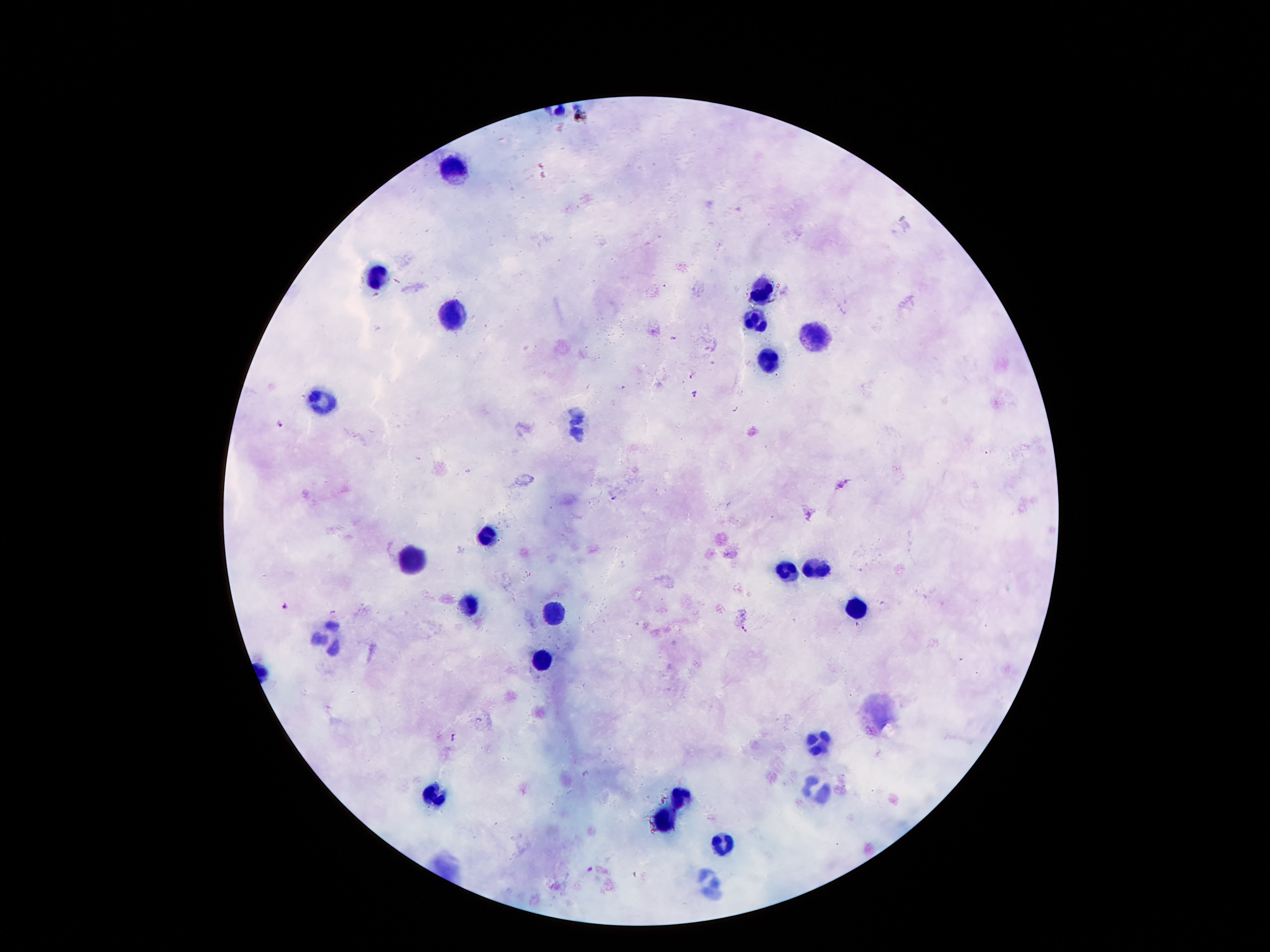

{
  "image_size": "1270×952 pixels",
  "patient_malaria_status": "positive for Plasmodium falciparum",
  "stain": "Giemsa",
  "capture": "smartphone through the microscope eyepiece",
  "malaria_parasite_locations": "approximate object centers, in pixels from the top-left corner: (x=673, y=337), (x=695, y=394), (x=280, y=423), (x=614, y=498), (x=285, y=605), (x=746, y=630), (x=453, y=737), (x=589, y=869)",
  "preparation": "thick peripheral-blood smear",
  "field_of_view": "one from this slide",
  "leukocyte_locations": "approximate object centers, in pixels from the top-left corner: (x=452, y=167), (x=377, y=276), (x=760, y=289), (x=450, y=314), (x=754, y=320), (x=818, y=336), (x=767, y=361), (x=322, y=400), (x=576, y=425), (x=487, y=537), (x=411, y=560), (x=815, y=566), (x=787, y=570), (x=467, y=603), (x=858, y=608), (x=550, y=612), (x=329, y=637), (x=541, y=659), (x=816, y=741), (x=815, y=791), (x=436, y=794), (x=680, y=799), (x=667, y=822), (x=724, y=843), (x=709, y=884)",
  "magnification": "100x"
}